Assess this cell for malaria.
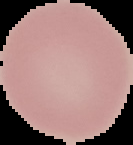

It is uninfected.

image_type: cell region segmented out of the field of view; surrounding area masked to black
preparation: thin blood smear
image_size: 133×145 pixels